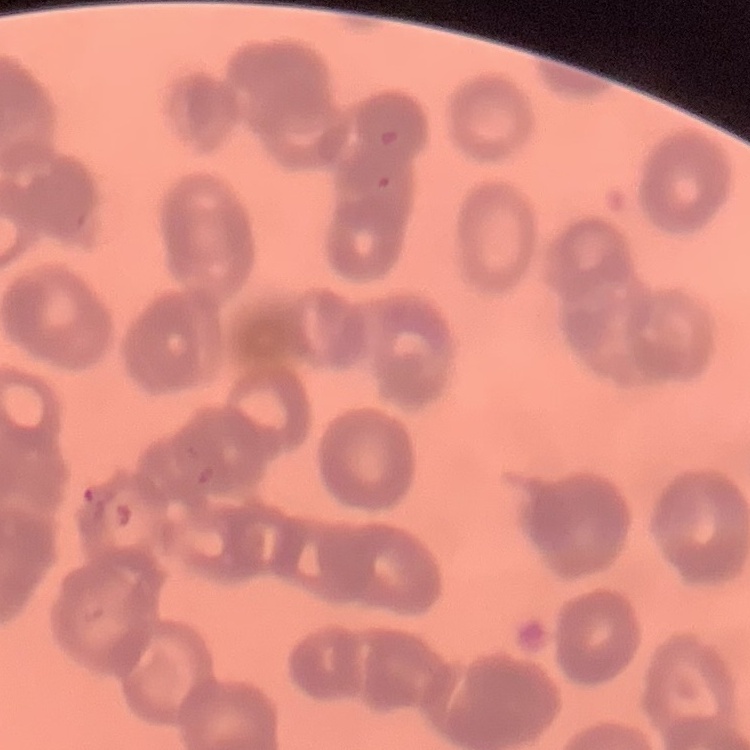

Summary:
  - Red blood cell morphology: rouleaux formation
  - Stain: Field's or Giemsa
  - Preparation: thin peripheral smear
  - Image type: square crop of a larger photomicrograph